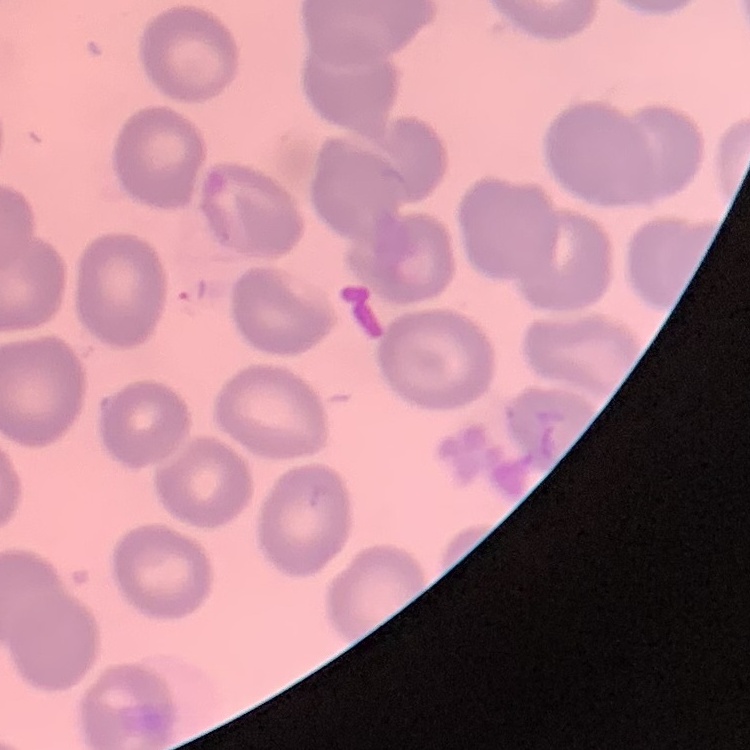
erythrocyte morphology = no rouleaux formation
preparation = thin blood smear
stain = Field's or Giemsa
image type = square crop of a larger photomicrograph